Classify this cell by malaria status.
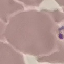
It is parasitized.

image type = automatically extracted cell patch, resized to 64 × 64 pixels
stain = Giemsa
capture = smartphone through the microscope eyepiece
preparation = thin blood smear